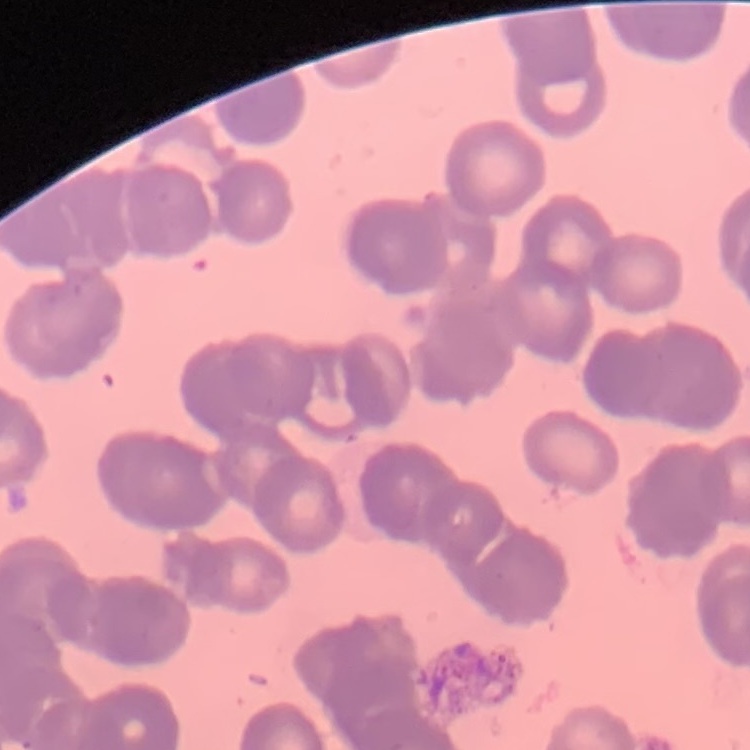 The red blood cells exhibit rouleaux formation. Stained with either Field's or Giemsa. Thin blood film. Square crop of a larger photomicrograph.